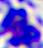 400x magnification. Photomicrograph. A white blood cell is shown.